Assess this cell for malaria.
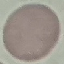

Uninfected.

stain: Giemsa
capture: smartphone camera at the microscope eyepiece
image_type: automatically extracted cell patch, resized to 64 × 64 pixels
preparation: thin smear